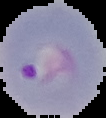

Summary:
  - Image type: segmented cell region with the area outside set to black
  - Malaria status: parasitized
  - Preparation: thin blood film
  - Image size: 106×118 pixels